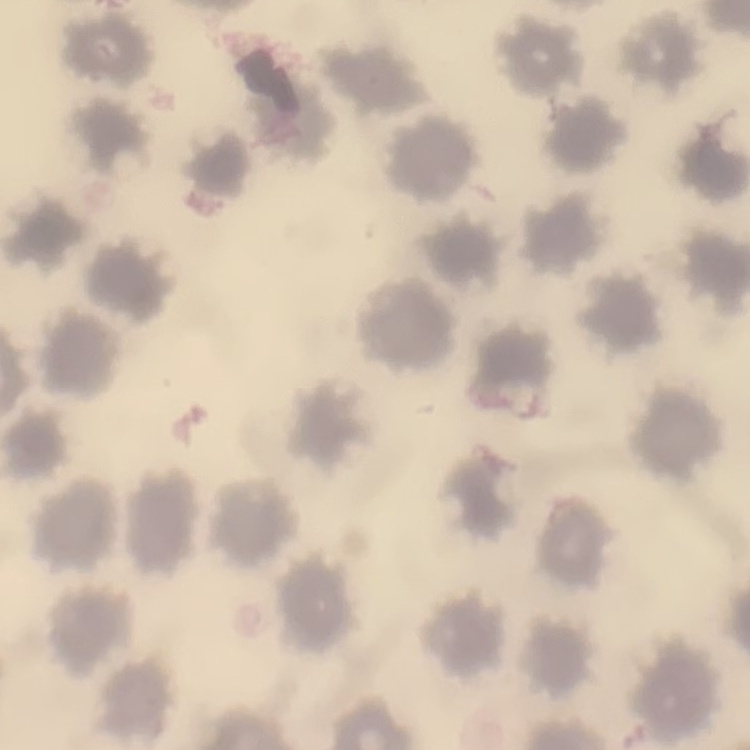

Summary:
  - Red blood cell morphology: no rouleaux formation
  - Preparation: thin peripheral smear
  - Stain: Field's or Giemsa
  - Image type: one tile cut from a larger photomicrograph